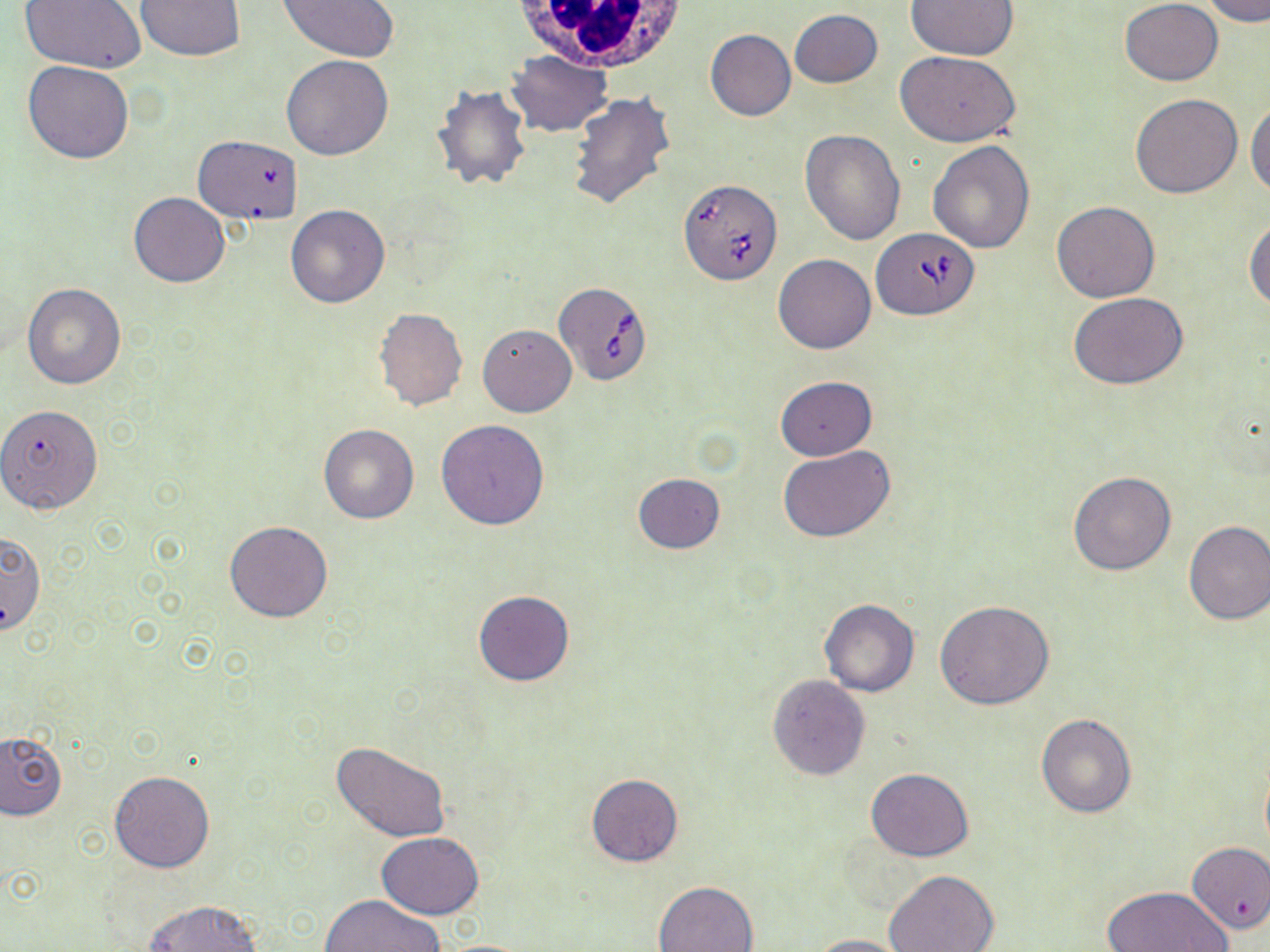
Summary:
  - Coordinate format: approximate bounding boxes as (x1, y1, x2, y2) in pixels
  - White blood cell locations: (509, 0, 689, 70)
  - Uninfected red blood cell locations: (19, 0, 147, 73), (135, 0, 246, 61), (277, 0, 400, 61), (904, 0, 1017, 59), (1119, 0, 1224, 86), (1201, 0, 1270, 26), (789, 9, 883, 88), (705, 29, 796, 121), (508, 51, 611, 136), (895, 51, 1023, 147), (281, 55, 394, 160), (23, 60, 134, 165), (432, 84, 531, 191), (568, 92, 676, 212), (1131, 94, 1242, 198), (1247, 102, 1270, 198), (800, 129, 906, 244), (192, 132, 305, 225), (927, 140, 1034, 253), (129, 191, 229, 288), (1051, 200, 1160, 302), (285, 204, 389, 310), (1244, 217, 1270, 312), (773, 253, 877, 354), (22, 283, 126, 389), (1069, 292, 1188, 389), (373, 306, 468, 411), (478, 323, 576, 417), (775, 375, 878, 461), (0, 403, 105, 513), (435, 419, 550, 529), (318, 424, 419, 524), (778, 446, 896, 543), (1068, 471, 1176, 575), (632, 474, 725, 554), (1183, 520, 1270, 626), (225, 521, 333, 623), (1, 531, 46, 635), (473, 589, 576, 687), (818, 599, 920, 696), (934, 600, 1055, 709), (767, 674, 868, 779), (1036, 714, 1136, 818), (0, 731, 66, 820), (331, 740, 451, 842), (865, 769, 975, 860), (109, 770, 215, 873), (586, 774, 684, 867), (377, 833, 486, 919), (1187, 841, 1270, 932), (883, 869, 999, 952), (653, 880, 760, 952), (1100, 886, 1233, 952), (320, 895, 446, 951), (144, 900, 261, 952), (809, 934, 913, 952)
  - Babesia divergens-infected red blood cell locations: (679, 179, 783, 284), (871, 229, 979, 320), (553, 280, 654, 386)
  - Slide-level diagnosis: Babesia divergens
  - Image size: 1270×952 pixels
  - Field of view: one of a larger specimen
  - Preparation: thin blood smear
  - Magnification: 1000x
  - Stain: May-Grünwald-Giemsa
  - Modality: light microscopy